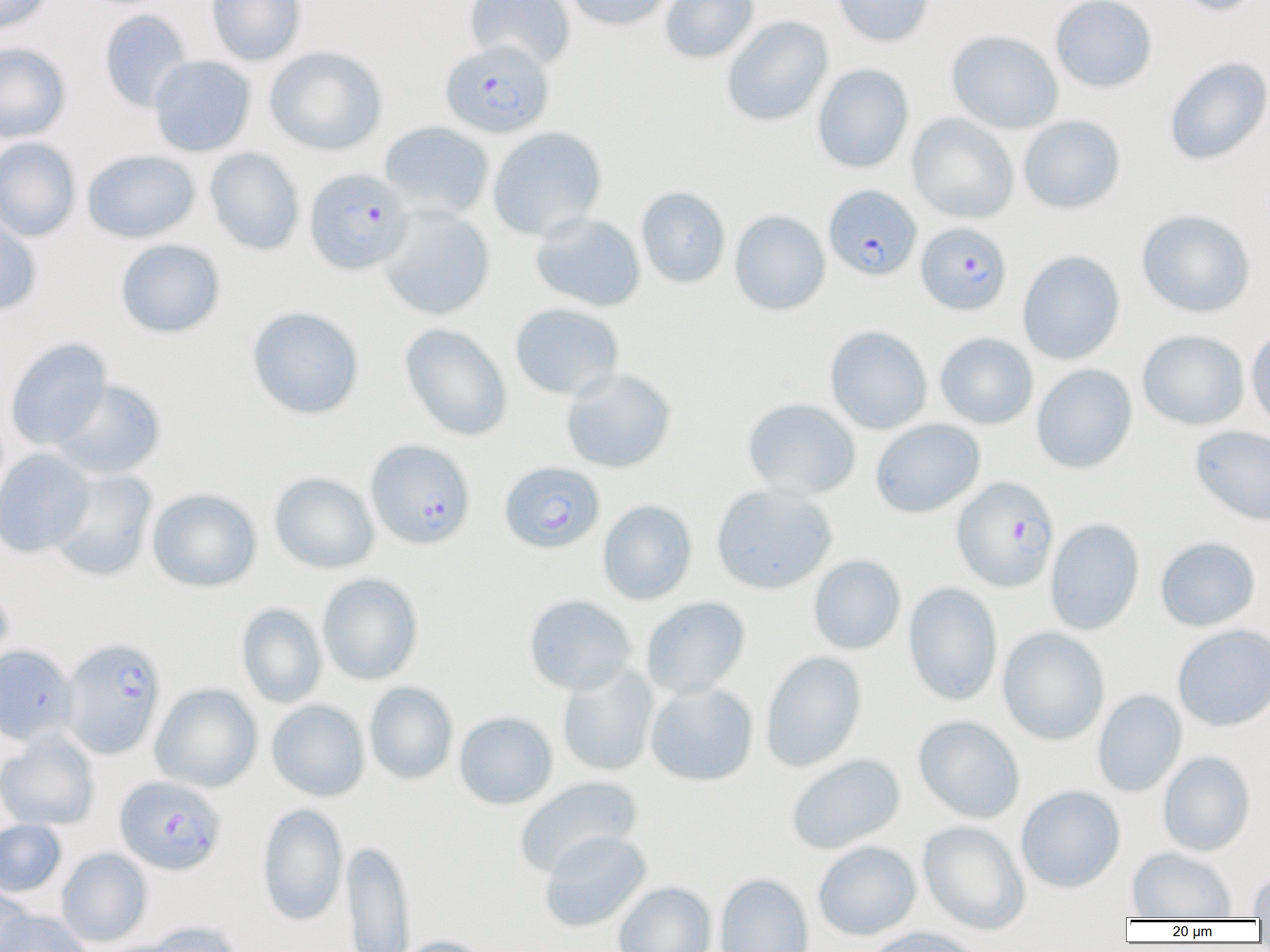

Approximate bounding boxes as (x1, y1, x2, y2) in pixels. Uninfected red blood cell locations (subset): (0, 0, 53, 34), (206, 0, 306, 65), (464, 0, 575, 70), (564, 0, 672, 30), (660, 0, 759, 63), (832, 0, 934, 46), (1050, 0, 1157, 92), (1174, 0, 1265, 16), (99, 9, 193, 112), (722, 16, 833, 126), (946, 30, 1063, 133), (0, 42, 71, 143), (265, 46, 387, 155), (148, 56, 256, 157), (1164, 56, 1270, 165), (812, 64, 914, 173), (907, 113, 1019, 224), (1018, 115, 1125, 213), (379, 121, 494, 220), (487, 126, 607, 240), (0, 137, 81, 242), (205, 148, 304, 255), (82, 149, 199, 243), (636, 186, 730, 289), (376, 205, 495, 320), (1136, 209, 1256, 317), (0, 210, 42, 315), (729, 210, 830, 315), (530, 212, 646, 312), (115, 239, 225, 338), (1017, 250, 1125, 365), (509, 303, 624, 400), (247, 306, 364, 419), (400, 323, 513, 441), (824, 325, 933, 434), (1246, 325, 1270, 432), (1137, 330, 1249, 430), (935, 332, 1038, 429), (5, 338, 112, 450), (1031, 364, 1137, 473), (560, 368, 677, 473), (50, 379, 166, 479), (742, 397, 862, 500), (870, 418, 986, 518), (1190, 425, 1270, 526), (0, 448, 94, 558), (48, 468, 157, 581), (269, 472, 379, 574), (711, 483, 837, 593), (147, 488, 262, 592), (597, 500, 697, 605), (1044, 518, 1145, 635), (1155, 536, 1260, 631), (808, 554, 906, 655), (316, 572, 424, 685), (903, 582, 1003, 705), (0, 586, 14, 677), (524, 594, 637, 695), (641, 597, 750, 698), (236, 603, 327, 708), (1172, 623, 1270, 731), (997, 626, 1110, 745), (760, 651, 867, 772), (557, 663, 659, 776), (364, 682, 458, 784), (645, 682, 758, 785), (150, 683, 262, 792), (1092, 689, 1187, 797), (266, 700, 370, 801), (454, 711, 557, 809), (914, 715, 1025, 823), (0, 732, 100, 831), (1157, 751, 1256, 856), (786, 753, 905, 854), (514, 776, 643, 877), (1015, 785, 1125, 893), (257, 803, 348, 926), (0, 819, 68, 897), (917, 819, 1030, 934), (539, 830, 651, 932), (342, 841, 415, 952), (812, 841, 922, 940), (56, 847, 153, 946), (1127, 847, 1237, 919), (1248, 865, 1270, 918), (715, 873, 814, 952), (613, 881, 717, 952), (0, 886, 33, 951), (1, 909, 94, 952), (140, 921, 242, 952), (862, 927, 985, 952), (394, 935, 490, 952). Plasmodium falciparum-infected red blood cell locations (subset): (440, 39, 553, 139), (304, 168, 414, 274), (823, 185, 921, 280), (916, 222, 1012, 315), (365, 439, 475, 549), (499, 461, 605, 553), (952, 476, 1059, 592), (61, 638, 166, 758), (114, 775, 226, 875). Slide-level diagnosis: Plasmodium falciparum. One field of a larger specimen. Light microscopy. Image is 1270×952 pixels. Thin blood smear. Captured at 1000x magnification.